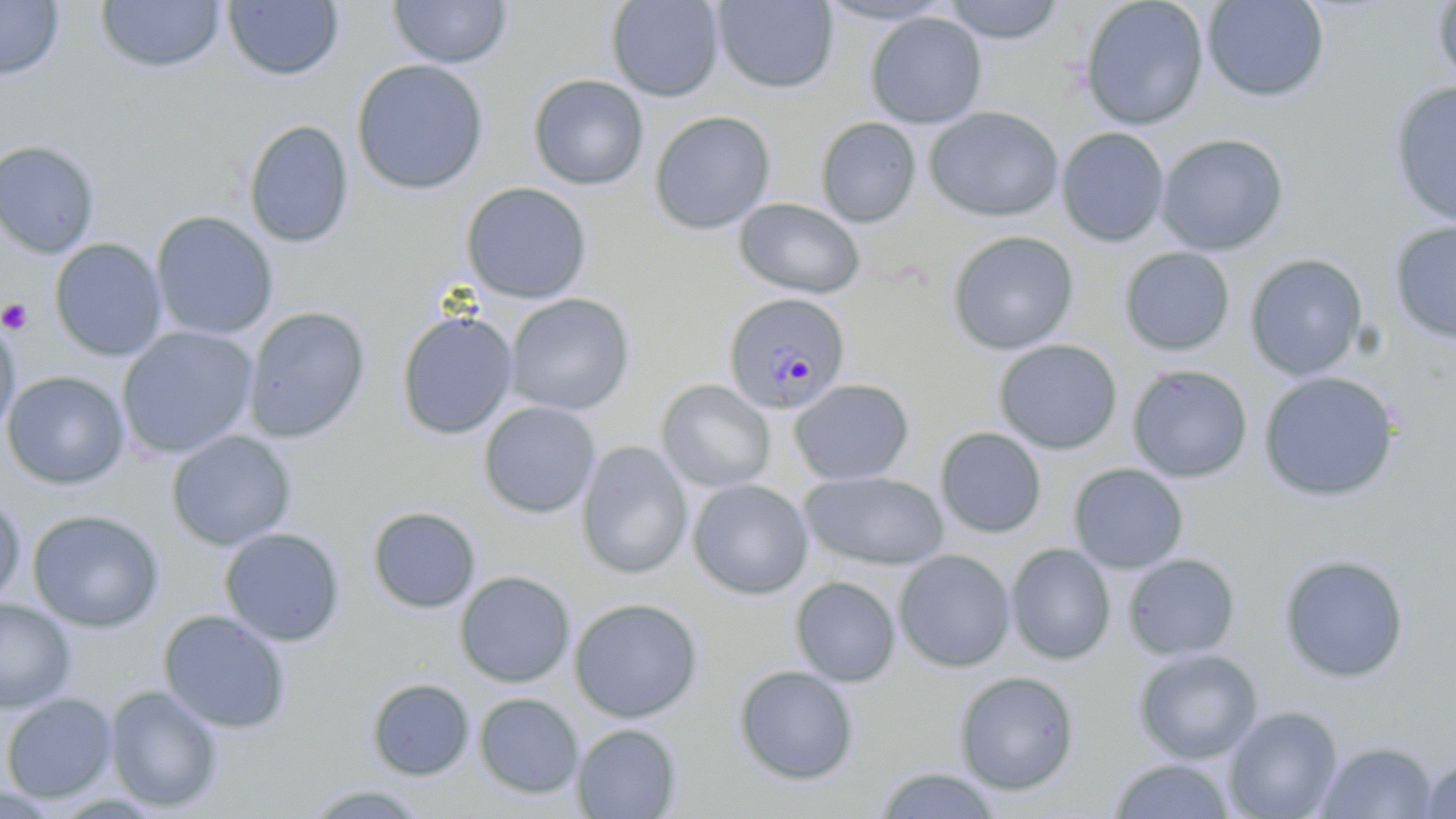

Approximate bounding boxes as named x1/y1/x2/y2 corners in pixels. Platelet locations: (x1=0, y1=298, x2=34, y2=333). Plasmodium malariae-infected red blood cell locations: (x1=722, y1=292, x2=852, y2=415). Uninfected red blood cell locations: (x1=0, y1=0, x2=65, y2=81), (x1=387, y1=0, x2=514, y2=69), (x1=605, y1=0, x2=725, y2=102), (x1=816, y1=0, x2=957, y2=26), (x1=941, y1=0, x2=1068, y2=44), (x1=1079, y1=0, x2=1209, y2=130), (x1=1202, y1=0, x2=1330, y2=103), (x1=95, y1=1, x2=226, y2=74), (x1=222, y1=1, x2=344, y2=81), (x1=712, y1=1, x2=839, y2=94), (x1=1430, y1=2, x2=1456, y2=88), (x1=865, y1=11, x2=987, y2=129), (x1=351, y1=58, x2=490, y2=196), (x1=527, y1=74, x2=649, y2=191), (x1=1388, y1=81, x2=1456, y2=228), (x1=924, y1=107, x2=1065, y2=222), (x1=648, y1=110, x2=776, y2=235), (x1=815, y1=117, x2=921, y2=227), (x1=243, y1=119, x2=354, y2=249), (x1=1056, y1=126, x2=1170, y2=246), (x1=1155, y1=133, x2=1289, y2=256), (x1=0, y1=139, x2=102, y2=258), (x1=461, y1=182, x2=592, y2=304), (x1=733, y1=198, x2=865, y2=299), (x1=150, y1=210, x2=278, y2=342), (x1=1387, y1=220, x2=1456, y2=345), (x1=946, y1=230, x2=1080, y2=355), (x1=50, y1=238, x2=168, y2=362), (x1=1118, y1=246, x2=1235, y2=356), (x1=1244, y1=253, x2=1368, y2=380), (x1=504, y1=293, x2=635, y2=416), (x1=243, y1=307, x2=371, y2=444), (x1=395, y1=310, x2=519, y2=440), (x1=0, y1=318, x2=21, y2=443), (x1=116, y1=326, x2=259, y2=461), (x1=993, y1=339, x2=1122, y2=454), (x1=1127, y1=365, x2=1253, y2=483), (x1=2, y1=370, x2=130, y2=490), (x1=1258, y1=371, x2=1401, y2=502), (x1=789, y1=378, x2=915, y2=487), (x1=655, y1=379, x2=776, y2=492), (x1=478, y1=401, x2=601, y2=518), (x1=935, y1=427, x2=1047, y2=539), (x1=165, y1=430, x2=298, y2=552), (x1=576, y1=441, x2=694, y2=579), (x1=1067, y1=463, x2=1190, y2=573), (x1=800, y1=471, x2=950, y2=571), (x1=686, y1=478, x2=813, y2=600), (x1=0, y1=493, x2=25, y2=606), (x1=367, y1=506, x2=481, y2=614), (x1=27, y1=509, x2=165, y2=632), (x1=219, y1=527, x2=345, y2=647), (x1=1005, y1=543, x2=1116, y2=664), (x1=893, y1=549, x2=1016, y2=672), (x1=1122, y1=553, x2=1241, y2=660), (x1=1277, y1=553, x2=1410, y2=684), (x1=454, y1=570, x2=575, y2=688), (x1=790, y1=575, x2=901, y2=687), (x1=568, y1=597, x2=704, y2=724), (x1=0, y1=598, x2=77, y2=713), (x1=157, y1=609, x2=292, y2=734), (x1=1132, y1=647, x2=1264, y2=763), (x1=733, y1=664, x2=860, y2=785), (x1=954, y1=670, x2=1080, y2=795), (x1=366, y1=678, x2=475, y2=781), (x1=104, y1=684, x2=225, y2=812), (x1=474, y1=692, x2=584, y2=799), (x1=0, y1=693, x2=119, y2=803), (x1=1222, y1=705, x2=1344, y2=819), (x1=571, y1=722, x2=683, y2=818), (x1=1315, y1=740, x2=1440, y2=819), (x1=1418, y1=757, x2=1456, y2=818), (x1=1105, y1=758, x2=1239, y2=818), (x1=872, y1=765, x2=1004, y2=819), (x1=297, y1=783, x2=436, y2=818). Slide-level diagnosis: Plasmodium malariae. Captured at 1000x magnification. May-Grünwald-Giemsa-stained preparation. Light microscopy. One field of a larger specimen. Image is 1456×819 pixels. Thin blood film.